Classify this cell by malaria status.
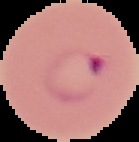

It is parasitized.

{
  "image_size": "139×142 pixels",
  "preparation": "thin blood film",
  "image_type": "cell region segmented out of the field of view; surrounding area masked to black"
}